Name the cell type shown.
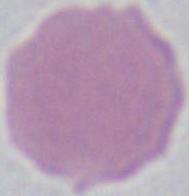
This is an erythrocyte.

Summary:
  - Magnification: 1000x
  - Modality: photomicrograph